Locate every uninfected red blood cell.
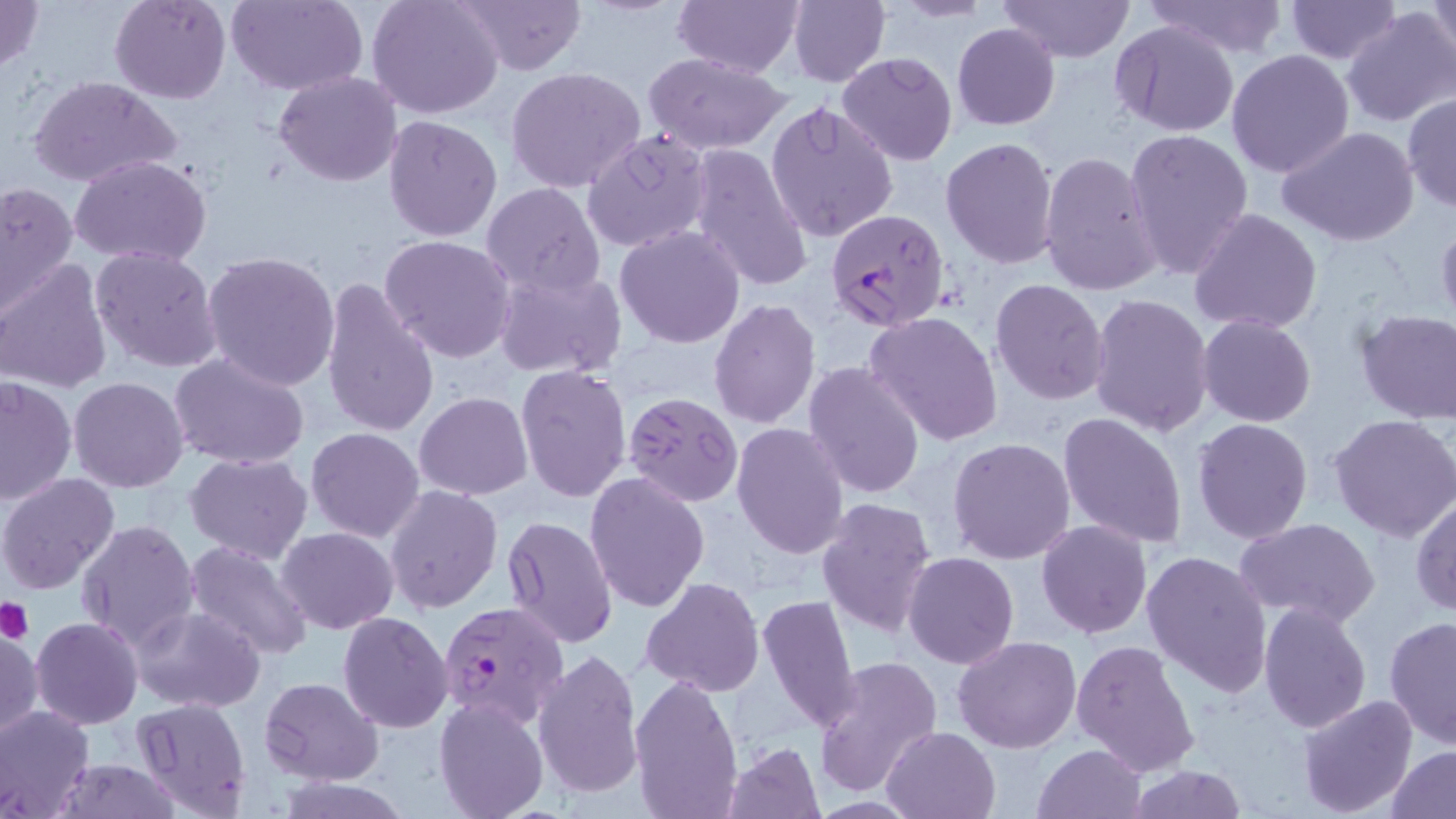

Approximate bounding boxes as (x1, y1, x2, y2) in pixels.
Uninfected red blood cells: (0, 0, 46, 78), (109, 0, 232, 104), (226, 0, 367, 95), (367, 0, 504, 120), (455, 0, 584, 74), (672, 0, 803, 78), (788, 0, 890, 87), (883, 0, 995, 22), (998, 0, 1134, 65), (1143, 0, 1290, 59), (1283, 0, 1401, 63), (1426, 0, 1456, 71), (1340, 5, 1456, 129), (1110, 22, 1239, 136), (951, 23, 1061, 131), (1226, 48, 1356, 177), (643, 51, 791, 155), (836, 52, 960, 166), (506, 66, 647, 195), (272, 70, 402, 186), (29, 75, 181, 189), (1401, 93, 1456, 213), (766, 100, 899, 242), (383, 116, 502, 241), (1275, 125, 1422, 247), (1124, 127, 1254, 277), (582, 131, 713, 253), (940, 136, 1059, 270), (684, 143, 816, 294), (1040, 151, 1162, 296), (69, 154, 214, 270), (0, 181, 79, 316), (481, 182, 606, 299), (1190, 207, 1323, 334), (1436, 217, 1456, 335), (614, 225, 746, 349), (378, 234, 517, 363), (90, 245, 222, 371), (202, 250, 341, 391), (0, 260, 114, 393), (494, 269, 624, 382), (320, 278, 441, 439), (990, 280, 1110, 406), (1089, 293, 1215, 438), (708, 297, 822, 431), (1355, 309, 1456, 423), (865, 311, 1004, 444), (1197, 314, 1316, 427), (168, 351, 310, 469), (804, 363, 926, 501), (515, 365, 632, 502), (0, 374, 77, 506), (69, 377, 190, 493), (415, 391, 531, 500), (624, 391, 744, 506), (1057, 410, 1188, 549), (1329, 412, 1456, 542), (1191, 419, 1313, 543), (732, 423, 850, 559), (305, 427, 425, 542), (947, 437, 1077, 565), (184, 452, 312, 564), (1, 473, 121, 594), (585, 473, 711, 612), (385, 485, 503, 613), (1410, 495, 1456, 618), (817, 496, 938, 637), (502, 515, 618, 648), (1235, 517, 1382, 628), (1037, 520, 1152, 638), (75, 521, 199, 650), (276, 526, 398, 634), (182, 540, 315, 660), (1141, 550, 1273, 699), (902, 552, 1019, 669), (641, 577, 765, 696), (758, 594, 860, 736), (1259, 601, 1372, 734), (130, 605, 266, 713), (337, 612, 453, 732), (30, 616, 143, 729), (1383, 616, 1456, 747), (0, 626, 41, 744), (952, 637, 1080, 754), (1071, 638, 1201, 778), (534, 645, 645, 800), (813, 656, 943, 799), (629, 673, 744, 818), (258, 677, 384, 786), (1297, 693, 1419, 816), (128, 696, 253, 819), (433, 699, 550, 819), (0, 704, 95, 818), (881, 724, 1002, 818), (720, 740, 826, 818), (1031, 743, 1146, 819), (1385, 745, 1455, 819), (50, 758, 185, 817), (1124, 764, 1247, 819), (275, 777, 413, 818).

Summary:
  - Platelet locations: (0, 599, 34, 644)
  - Plasmodium falciparum-infected red blood cell locations: (827, 207, 952, 331), (435, 599, 569, 730)
  - Slide-level diagnosis: Plasmodium falciparum
  - Magnification: 1000x
  - Preparation: thin blood film
  - Image size: 1456×819 pixels
  - Stain: May-Grünwald-Giemsa
  - Modality: optical microscopy
  - Field of view: one of a larger specimen